Identify the blood parasite species.
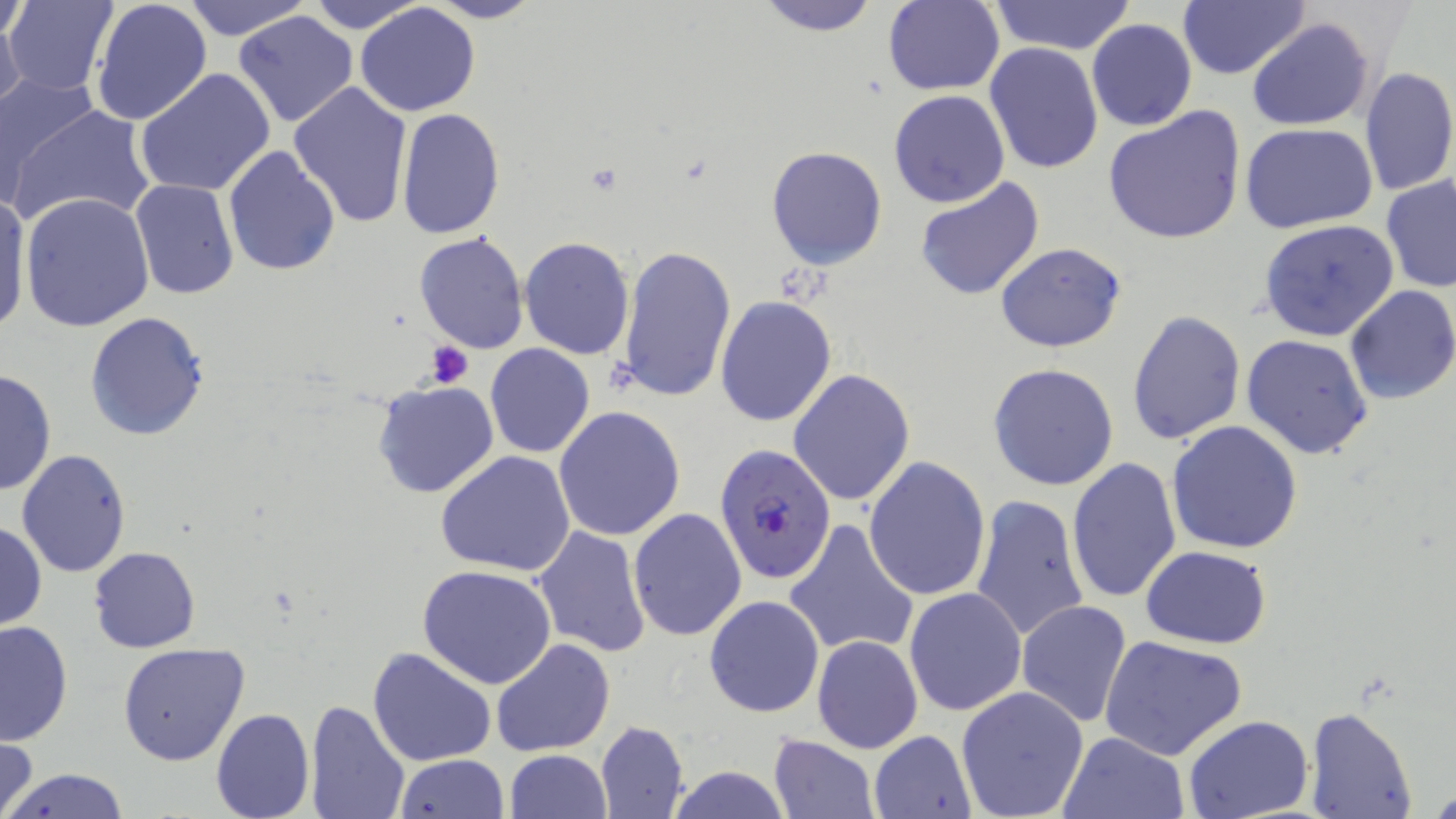
Plasmodium falciparum.

magnification = 1000x
Plasmodium falciparum-infected red blood cell locations = approximate bounding boxes as (x1,y1)-(x2,y2) corner pairs in pixels: (713,443)-(836,582)
image size = 1456×819 pixels
field of view = single
modality = optical microscopy
preparation = thin blood smear
platelet locations = approximate bounding boxes as (x1,y1)-(x2,y2) corner pairs in pixels: (422,340)-(476,390)
stain = May-Grünwald-Giemsa
uninfected red blood cell locations = approximate bounding boxes as (x1,y1)-(x2,y2) corner pairs in pixels: (5,0)-(122,96), (91,0)-(214,125), (180,0)-(312,41), (302,0)-(431,34), (421,0)-(543,24), (753,0)-(882,36), (987,0)-(1139,55), (881,1)-(1005,95), (1176,1)-(1309,80), (0,2)-(30,48), (354,3)-(482,116), (0,6)-(27,109), (233,10)-(360,127), (1247,17)-(1375,132), (1087,18)-(1196,131), (984,42)-(1104,175), (1359,66)-(1456,198), (134,68)-(275,198), (0,69)-(100,205), (288,81)-(413,228), (888,90)-(1011,209), (12,102)-(157,230), (394,108)-(505,241), (1104,108)-(1248,245), (1240,123)-(1379,235), (223,146)-(342,280), (767,146)-(888,269), (913,175)-(1045,301), (1381,176)-(1456,293), (130,179)-(239,300), (19,191)-(155,332), (0,192)-(32,338), (1259,218)-(1400,342), (414,232)-(528,354), (520,236)-(634,358), (995,241)-(1127,351), (618,245)-(737,406), (1343,285)-(1456,405), (715,296)-(837,427), (1127,310)-(1247,446), (84,311)-(212,443), (1242,334)-(1373,460), (484,344)-(595,458), (987,364)-(1119,491), (0,369)-(56,499), (790,369)-(914,506), (371,380)-(499,500), (554,406)-(686,542), (1167,420)-(1304,555), (16,448)-(132,578), (435,451)-(576,577), (1065,455)-(1180,605), (863,456)-(991,600), (969,492)-(1089,645), (628,507)-(747,642), (784,519)-(919,658), (0,522)-(47,631), (532,526)-(651,659), (1140,544)-(1274,649), (89,546)-(199,653), (416,564)-(556,689), (904,587)-(1027,717), (703,595)-(825,718), (1016,600)-(1132,727), (0,620)-(74,746), (812,634)-(923,753), (1099,634)-(1248,760), (491,638)-(618,755), (118,642)-(249,766), (367,646)-(498,767), (956,686)-(1090,819), (306,699)-(411,819), (210,706)-(315,819), (1303,707)-(1417,819), (1183,716)-(1316,819), (596,720)-(689,819), (869,730)-(976,818), (1057,732)-(1189,819), (767,733)-(878,818), (0,734)-(39,819), (504,749)-(613,818), (392,754)-(508,819), (665,766)-(793,819), (5,767)-(131,819)